State the blood parasite species.
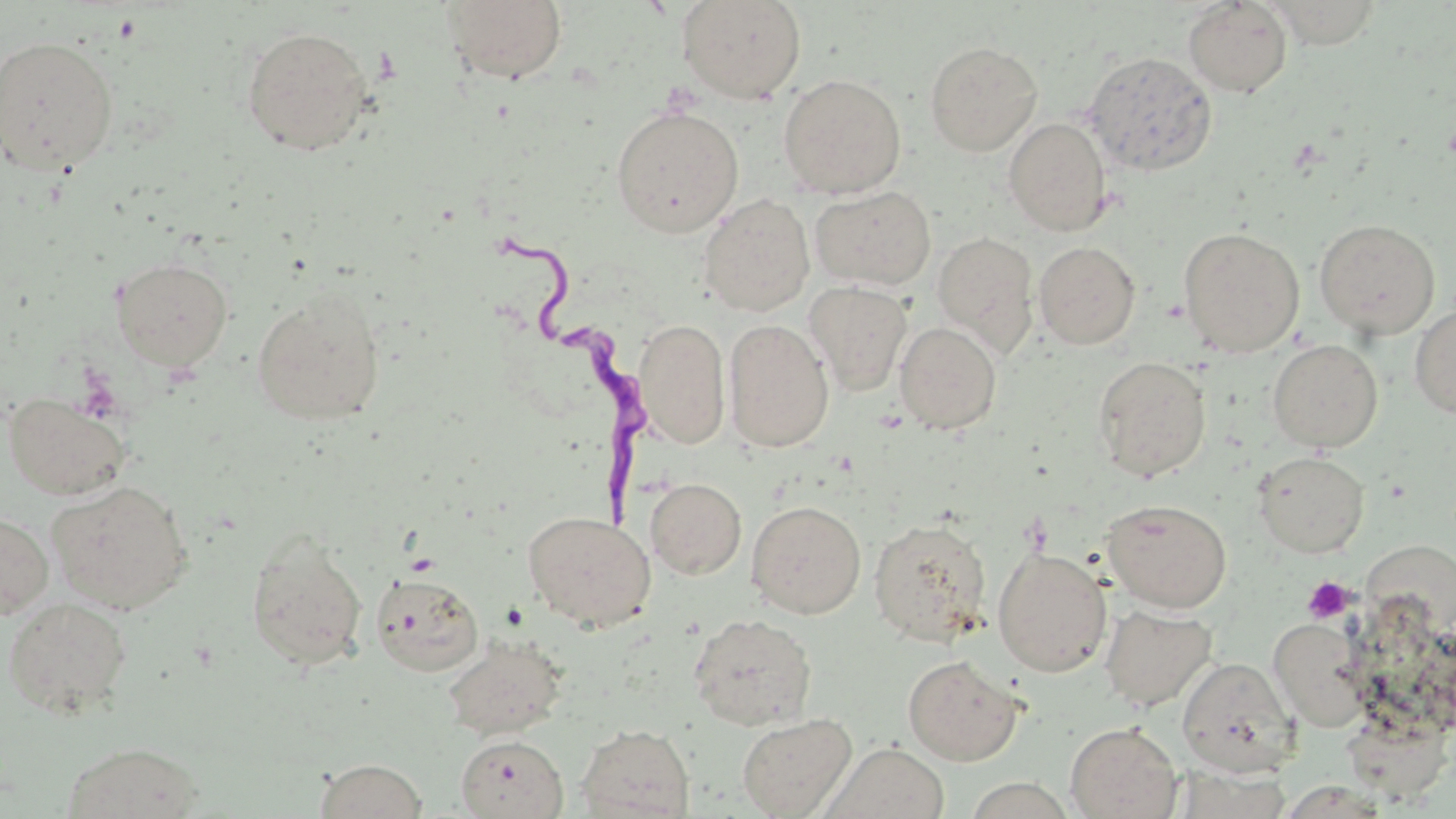

Trypanosoma brucei.

Approximate bounding boxes as (x1, y1, x2, y2) in pixels. Uninfected red blood cell locations: (440, 0, 568, 85), (676, 0, 807, 104), (1183, 1, 1293, 98), (1262, 1, 1386, 49), (241, 25, 374, 156), (0, 34, 119, 176), (925, 41, 1042, 156), (1083, 50, 1218, 177), (778, 73, 906, 199), (610, 105, 744, 237), (1004, 117, 1112, 236), (810, 185, 936, 290), (698, 193, 815, 316), (1314, 219, 1441, 338), (1178, 226, 1305, 357), (932, 232, 1039, 355), (1034, 241, 1140, 349), (110, 256, 234, 371), (804, 281, 912, 396), (251, 287, 387, 426), (1410, 304, 1456, 418), (634, 318, 730, 448), (723, 318, 834, 452), (895, 321, 1002, 435), (1267, 339, 1383, 452), (1093, 356, 1211, 481), (2, 391, 131, 501), (1253, 451, 1370, 558), (645, 477, 747, 579), (46, 480, 193, 614), (1103, 498, 1232, 613), (746, 500, 866, 618), (0, 510, 54, 619), (522, 510, 656, 632), (868, 518, 992, 646), (245, 530, 368, 670), (992, 546, 1112, 677), (370, 571, 484, 676), (2, 597, 133, 717), (1100, 605, 1217, 711), (688, 613, 817, 730), (1269, 619, 1371, 731), (443, 635, 567, 740), (903, 655, 1024, 765), (1177, 656, 1297, 777), (737, 712, 857, 818), (1065, 722, 1182, 819), (576, 723, 695, 818), (456, 734, 568, 818), (60, 741, 205, 819), (823, 742, 951, 819), (313, 759, 428, 818). Trypanosoma brucei locations: (493, 238, 654, 530). Platelet locations: (1302, 576, 1356, 624). Captured at 1000x magnification. One field of a larger specimen. Light microscopy. Thin blood film. Image is 1456×819 pixels. May-Grünwald-Giemsa stain.